Identify the cell.
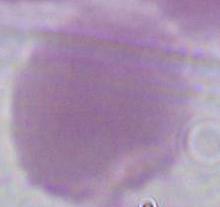

This is an erythrocyte.

Summary:
  - Magnification: 1000x
  - Modality: micrograph